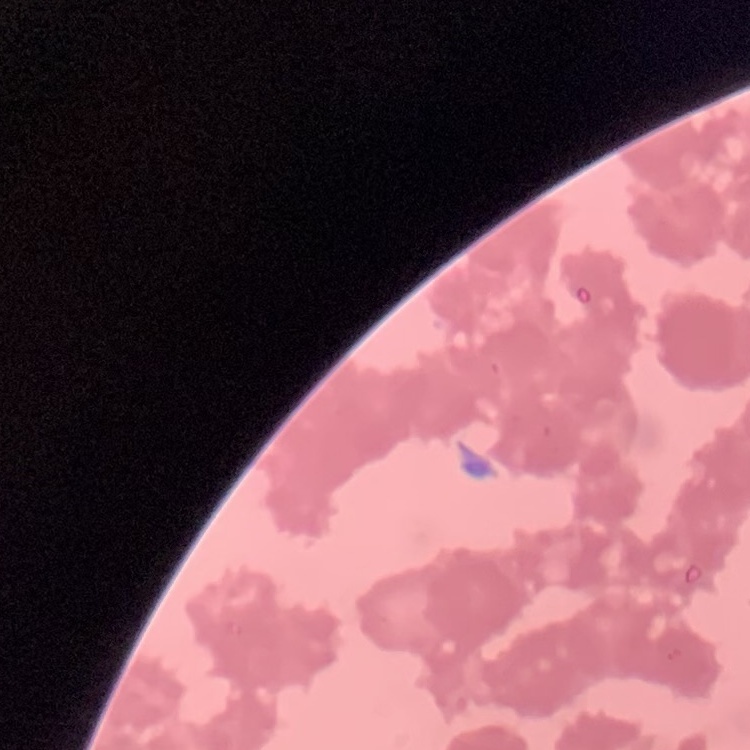

The erythrocytes exhibit rouleaux formation. Square crop of a larger photomicrograph. Thin blood film. Stained with either Field's or Giemsa.